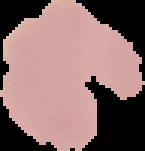

Summary:
  - Preparation: thin blood film
  - Result: negative for Plasmodium parasites
  - Image size: 145×151 pixels
  - Image type: segmented cell region with the area outside set to black